Outline platelets.
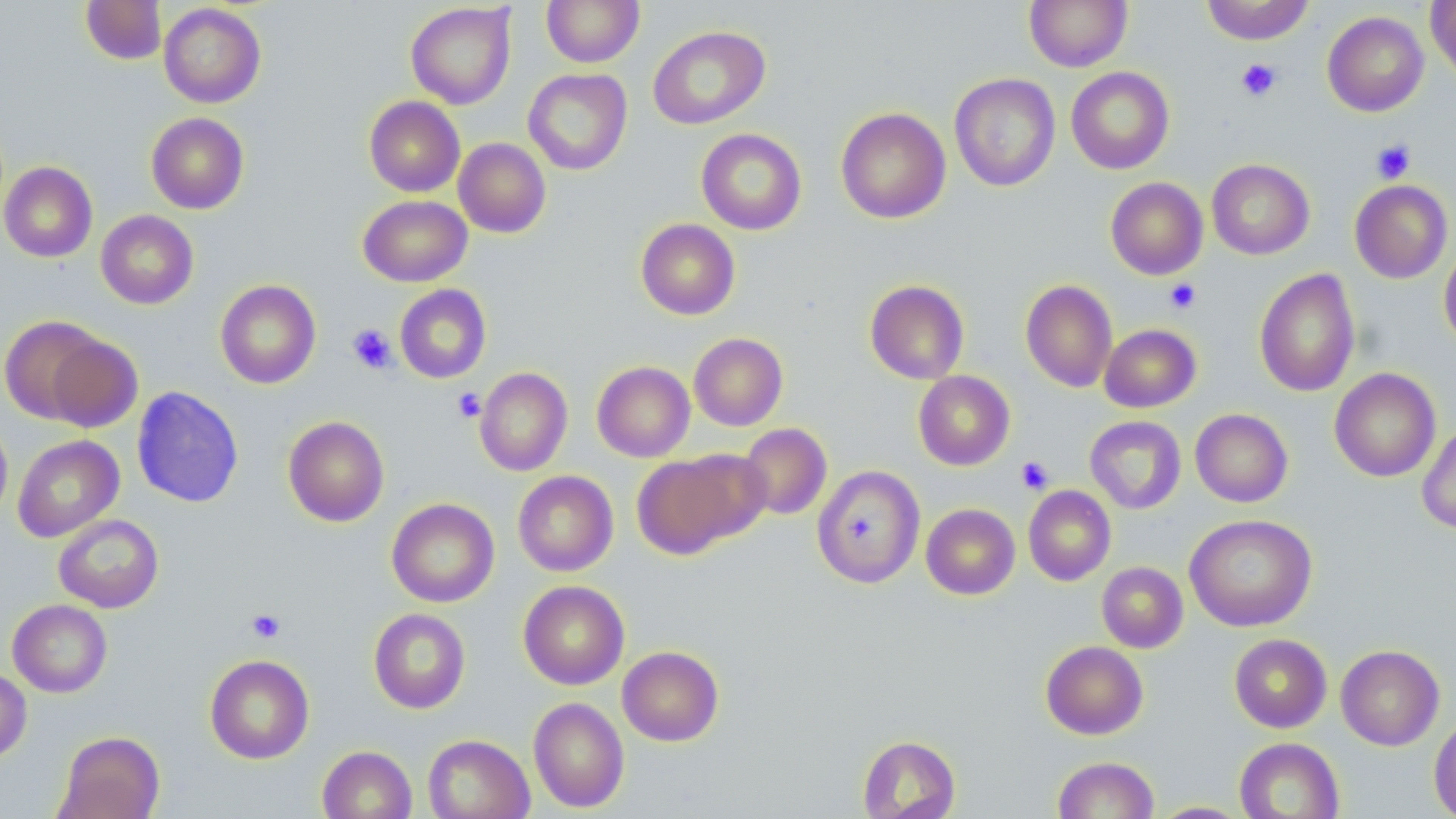
Approximate bounding boxes as (x1, y1, x2, y2) in pixels.
Platelets: (1236, 58, 1282, 102), (1371, 139, 1416, 183), (1165, 278, 1201, 313), (347, 323, 397, 374), (452, 389, 485, 422), (1016, 456, 1054, 495), (245, 608, 286, 644).

slide_level_diagnosis: no evidence of blood parasites
preparation: thin blood film
modality: light microscopy
image_size: 1456×819 pixels
magnification: 1000x
uninfected_red_blood_cell_locations: 'approximate bounding boxes as (x1, y1, x2, y2) in pixels: (541, 0, 644, 67), (1024, 0, 1132, 72), (1201, 0, 1314, 45), (1426, 0, 1456, 84), (81, 1, 166, 65), (158, 3, 266, 108), (405, 3, 517, 109), (1322, 11, 1429, 117), (647, 25, 770, 130), (1065, 67, 1174, 174), (523, 68, 633, 175), (949, 73, 1061, 192), (364, 96, 465, 197), (835, 106, 951, 224), (146, 112, 249, 214), (696, 129, 807, 235), (454, 138, 551, 238), (1207, 158, 1315, 260), (0, 161, 98, 262), (1105, 177, 1208, 280), (1350, 180, 1453, 283), (358, 195, 472, 287), (95, 210, 199, 309), (635, 218, 740, 320), (1439, 242, 1456, 351), (1254, 267, 1360, 397), (215, 279, 321, 389), (1020, 279, 1118, 392), (865, 280, 969, 384), (394, 285, 491, 383), (1, 315, 109, 424), (1099, 324, 1201, 412), (689, 333, 788, 431), (45, 335, 142, 433), (592, 361, 695, 462), (474, 367, 572, 476), (1329, 368, 1441, 482), (913, 371, 1015, 471), (131, 386, 244, 507), (1190, 408, 1293, 507), (283, 415, 389, 527), (1085, 416, 1186, 514), (0, 417, 13, 525), (739, 423, 832, 520), (1416, 424, 1456, 534), (12, 435, 124, 542), (673, 449, 773, 544), (632, 454, 746, 560), (812, 465, 925, 589), (513, 470, 618, 576), (1023, 485, 1116, 585), (386, 498, 500, 607), (921, 503, 1020, 599), (53, 514, 164, 613), (1184, 514, 1318, 632), (1097, 562, 1188, 652), (518, 580, 630, 690), (8, 599, 112, 698), (369, 608, 470, 714), (1229, 633, 1332, 733), (1230, 639, 1443, 738), (1040, 641, 1148, 739), (1336, 644, 1444, 750), (617, 646, 724, 746), (204, 654, 315, 764), (0, 666, 32, 763), (528, 696, 629, 813), (1428, 713, 1456, 818), (57, 730, 165, 819), (422, 734, 535, 819), (857, 735, 960, 819), (1234, 737, 1344, 818), (317, 745, 417, 819), (1052, 756, 1159, 819), (1148, 802, 1252, 818)'
stain: May-Grünwald-Giemsa
field_of_view: one of a larger specimen